Identify the parasite.
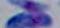
Toxoplasma gondii.

Summary:
  - Modality: photomicrograph
  - Magnification: 1000x